Comment on the morphology of the erythrocytes.
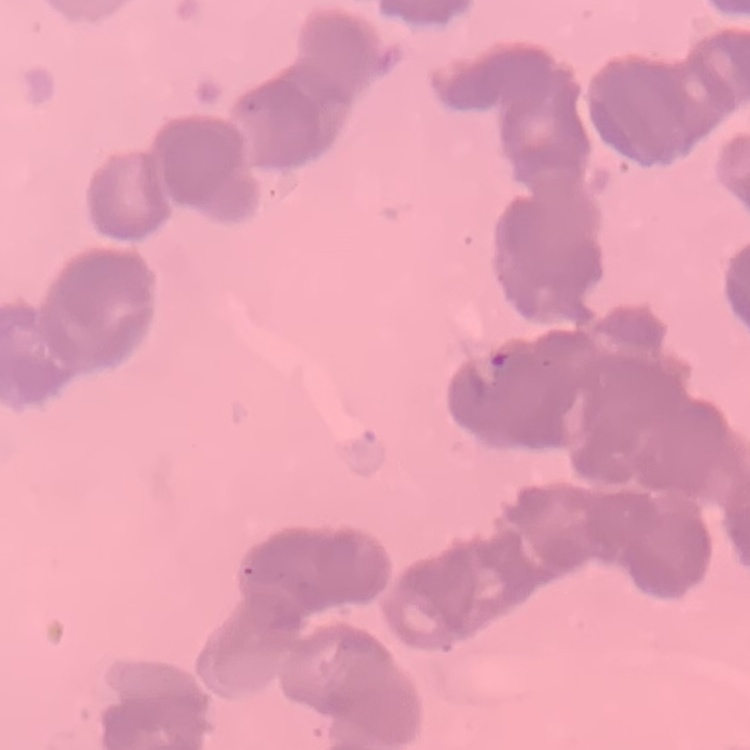

They show rouleaux formation.

Summary:
  - Stain: Field's or Giemsa
  - Image type: one tile cut from a larger photomicrograph
  - Preparation: thin blood film